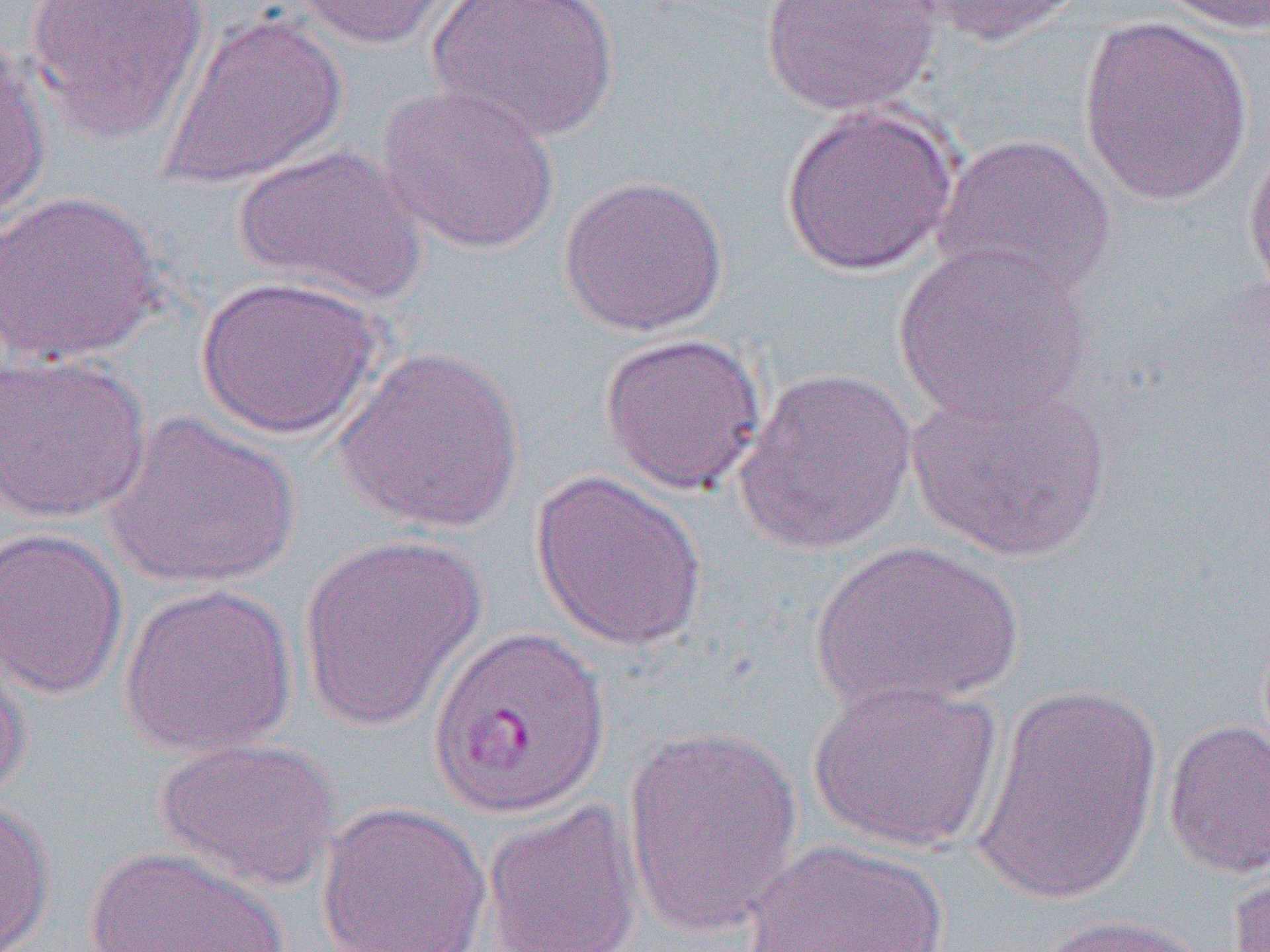 Approximate bounding boxes as named x1/y1/x2/y2 corners in pixels. Uninfected red blood cell locations: (x1=25, y1=0, x2=212, y2=144), (x1=289, y1=0, x2=458, y2=51), (x1=427, y1=0, x2=620, y2=144), (x1=760, y1=0, x2=944, y2=116), (x1=903, y1=0, x2=1089, y2=46), (x1=1154, y1=0, x2=1270, y2=35), (x1=159, y1=11, x2=349, y2=191), (x1=1078, y1=14, x2=1254, y2=206), (x1=0, y1=37, x2=52, y2=219), (x1=376, y1=84, x2=561, y2=256), (x1=778, y1=105, x2=960, y2=278), (x1=932, y1=132, x2=1118, y2=304), (x1=1244, y1=135, x2=1270, y2=312), (x1=231, y1=142, x2=429, y2=308), (x1=558, y1=173, x2=730, y2=338), (x1=0, y1=189, x2=166, y2=367), (x1=893, y1=241, x2=1095, y2=428), (x1=195, y1=274, x2=384, y2=441), (x1=598, y1=332, x2=767, y2=495), (x1=334, y1=344, x2=525, y2=535), (x1=0, y1=351, x2=152, y2=525), (x1=732, y1=366, x2=918, y2=556), (x1=905, y1=379, x2=1116, y2=564), (x1=101, y1=410, x2=302, y2=590), (x1=529, y1=469, x2=709, y2=652), (x1=0, y1=527, x2=129, y2=701), (x1=297, y1=534, x2=487, y2=732), (x1=808, y1=540, x2=1023, y2=713), (x1=117, y1=583, x2=298, y2=758), (x1=0, y1=646, x2=32, y2=806), (x1=807, y1=676, x2=1005, y2=855), (x1=973, y1=680, x2=1164, y2=909), (x1=1163, y1=719, x2=1270, y2=879), (x1=621, y1=725, x2=804, y2=940), (x1=153, y1=737, x2=341, y2=894), (x1=482, y1=799, x2=645, y2=952), (x1=0, y1=800, x2=57, y2=951), (x1=316, y1=801, x2=492, y2=952), (x1=741, y1=838, x2=958, y2=952), (x1=81, y1=845, x2=292, y2=952), (x1=1227, y1=860, x2=1270, y2=952), (x1=1032, y1=913, x2=1215, y2=952). Slide-level diagnosis: Plasmodium vivax. Image is 1270×952 pixels. Optical microscopy. Single field of view. 1000x magnification. Thin blood film.